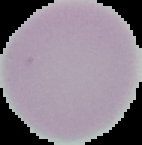

malaria status = uninfected
preparation = thin blood film
image type = cell region segmented out of the field of view; surrounding area masked to black
image size = 142×145 pixels